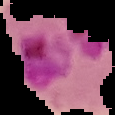 Image is 115×115 pixels. From a thin blood film. Cell region segmented out of the field of view; the surrounding area is masked to black. Malaria status: parasitized.